Report the malaria status of this cell.
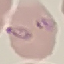
It is parasitized.

{
  "image_type": "automatically extracted cell patch, resized to 64 × 64 pixels",
  "capture": "smartphone camera at the microscope eyepiece",
  "stain": "Giemsa",
  "preparation": "thin smear"
}